Assess the morphology of the red blood cells.
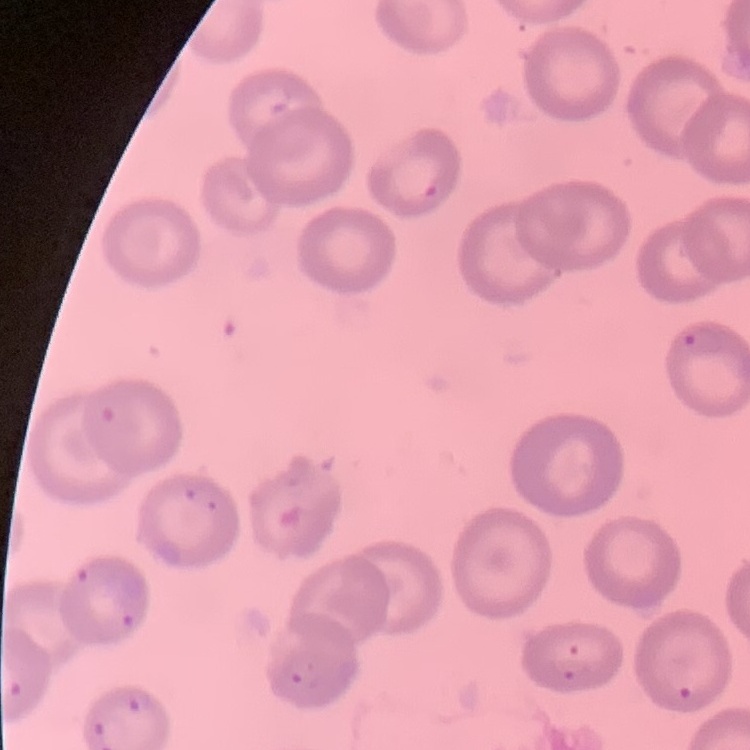
No rouleaux formation.

Field's or Giemsa stain. One tile cut from a larger photomicrograph. Thin blood film.